Comment on the morphology of the red blood cells.
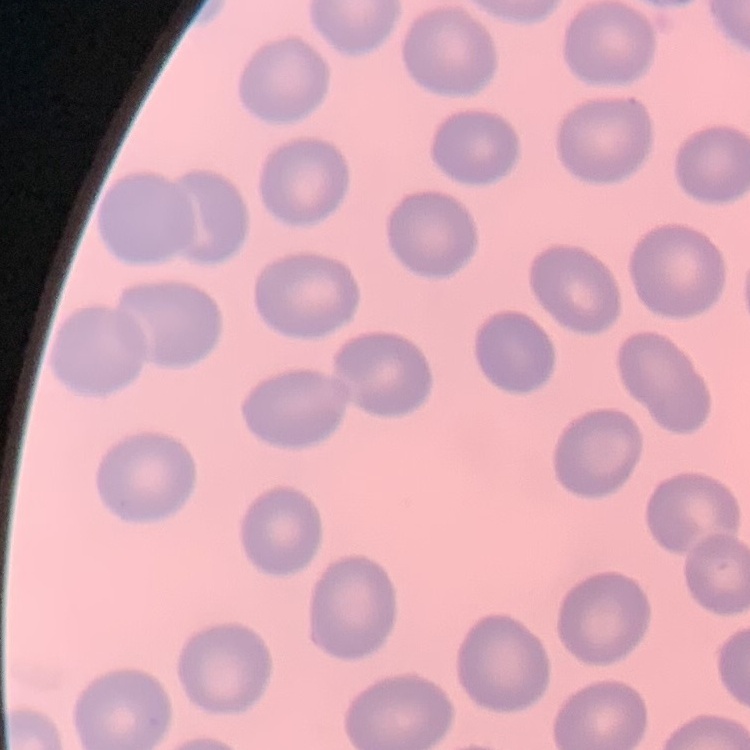

No rouleaux formation.

Summary:
  - Image type: one tile cut from a larger photomicrograph
  - Stain: Field's or Giemsa
  - Preparation: thin peripheral smear